Locate every Plasmodium parasite.
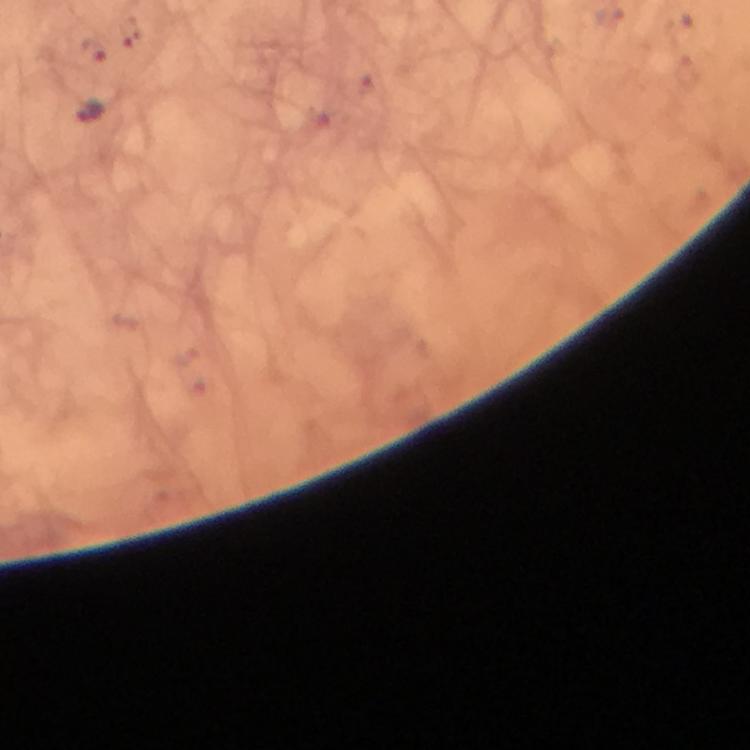

Approximate centers as {x, y} in pixels.
Plasmodium parasites: {90, 111}.

100x magnification. Thick smear. Giemsa-stained preparation. A crop from one field of view. Immersion oil applied. Photographed through the microscope with a smartphone camera. Image is 750×750 pixels. From a diagnostic examination for malaria.